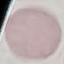

Result: negative for malaria parasites. Acquired by smartphone through the microscope eyepiece. Thin smear of blood. Automatically extracted cell patch, resized to 64 × 64 pixels. Giemsa stain.